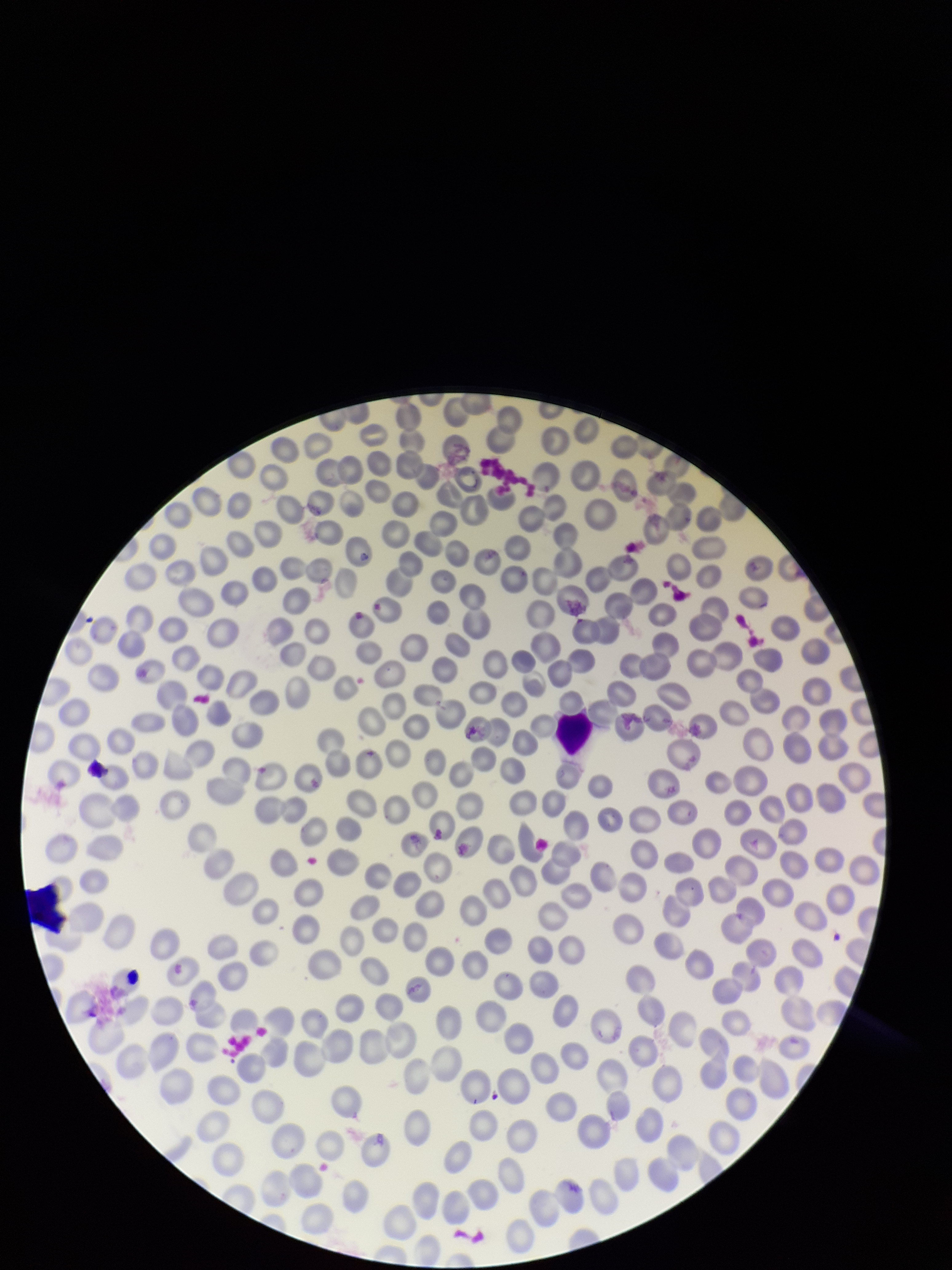 Image is 952×1270 pixels. Stained with Giemsa. Red blood cell count: 278. Parasitized red blood cell count: 0. Preparation: thin smear. Photographed through the microscope eyepiece with a smartphone camera. Single field of view. Patient malaria status: negative. Parasitized red blood cells: none detected.